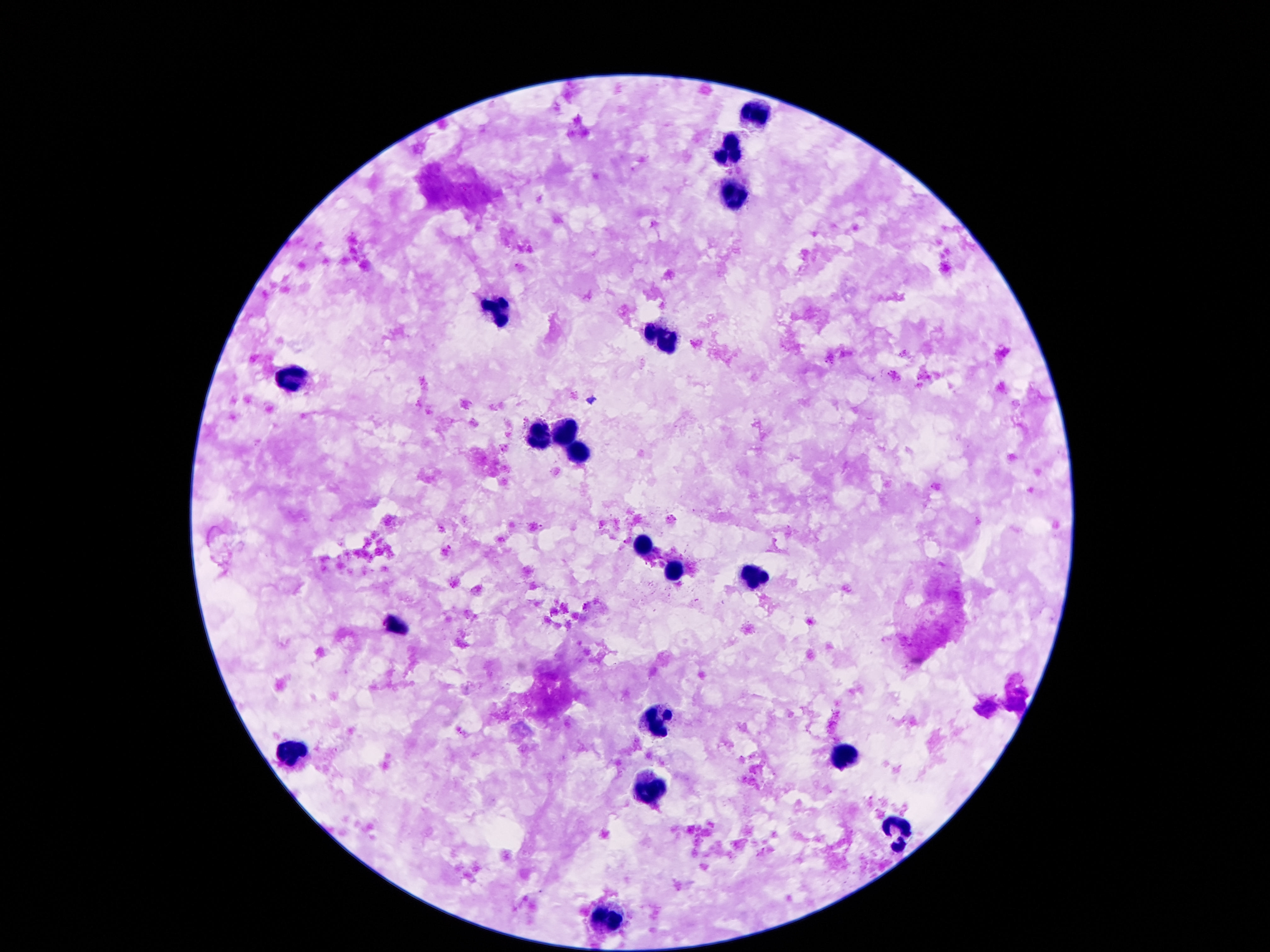

Approximate centers as [x, y] in pixels.
Summary:
  - Leukocyte locations: [748, 114], [725, 157], [734, 197], [494, 312], [655, 337], [287, 381], [561, 431], [534, 440], [579, 451], [643, 549], [675, 573], [754, 578], [396, 623], [655, 722], [846, 757], [292, 759], [653, 792], [897, 828], [606, 922]
  - Capture: smartphone camera through the microscope eyepiece
  - Field of view: one from this slide
  - Magnification: 100x
  - Preparation: thick blood film
  - Image size: 1270×952 pixels
  - Stain: Giemsa
  - Patient malaria status: not infected